Assess this cell for malaria.
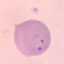
Parasitized.

capture: smartphone camera at the microscope eyepiece
stain: Giemsa
image_type: automatically extracted cell patch, resized to 64 × 64 pixels
preparation: thin blood smear